Outline each blood parasite and name the species.
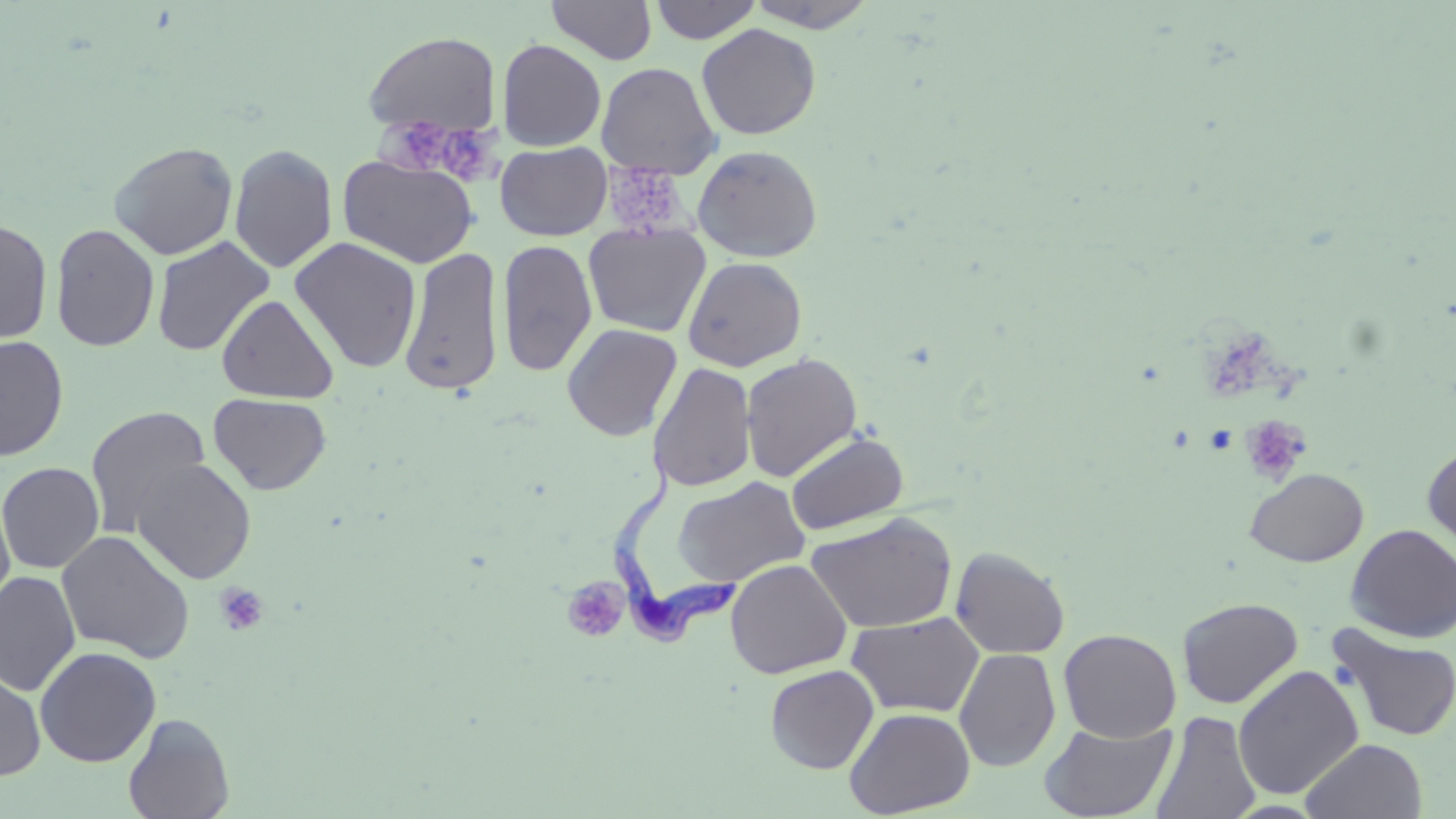
Approximate bounding boxes as (x1, y1, x2, y2) in pixels.
Trypanosoma brucei: (608, 443, 738, 655).
No Plasmodium falciparum, Plasmodium ovale, Plasmodium malariae, Plasmodium vivax, or Babesia divergens observed.

Summary:
  - Uninfected red blood cell locations: (547, 0, 657, 64), (649, 0, 762, 44), (745, 0, 879, 32), (696, 23, 821, 141), (363, 30, 501, 139), (496, 39, 607, 151), (596, 62, 721, 178), (108, 141, 238, 260), (495, 141, 612, 241), (228, 143, 338, 274), (692, 144, 823, 263), (338, 154, 480, 268), (0, 218, 53, 344), (583, 222, 710, 338), (50, 223, 160, 352), (151, 236, 275, 356), (289, 236, 423, 373), (496, 238, 596, 378), (398, 246, 505, 397), (683, 256, 807, 372), (217, 294, 339, 404), (562, 323, 683, 441), (0, 334, 69, 461), (740, 352, 862, 482), (647, 361, 757, 493), (208, 393, 331, 495), (85, 405, 211, 537), (785, 430, 908, 536), (1422, 442, 1456, 557), (131, 458, 257, 584), (0, 461, 105, 573), (1245, 467, 1369, 567), (673, 476, 810, 589), (0, 487, 16, 615), (806, 513, 956, 634), (1345, 523, 1456, 643), (56, 529, 196, 664), (950, 547, 1070, 659), (725, 559, 852, 679), (0, 570, 80, 696), (1177, 596, 1303, 709), (846, 612, 984, 718), (1326, 623, 1456, 743), (1058, 628, 1182, 742), (35, 646, 161, 767), (953, 648, 1061, 772), (0, 664, 46, 779), (765, 664, 879, 774), (1233, 665, 1364, 801), (844, 706, 975, 817), (1151, 710, 1261, 819), (123, 713, 235, 819), (1039, 719, 1176, 819), (1301, 738, 1428, 818)
  - Platelet locations: (372, 114, 445, 174), (443, 123, 511, 189), (603, 160, 700, 238), (1211, 324, 1309, 402), (1240, 415, 1312, 485), (562, 578, 631, 643), (214, 582, 270, 636)
  - Slide-level diagnosis: Trypanosoma brucei
  - Field of view: single
  - Preparation: thin blood film
  - Stain: May-Grünwald-Giemsa
  - Magnification: 1000x
  - Modality: light microscopy
  - Image size: 1456×819 pixels